Give the extent of all Plasmodium falciparum-infected red blood cells.
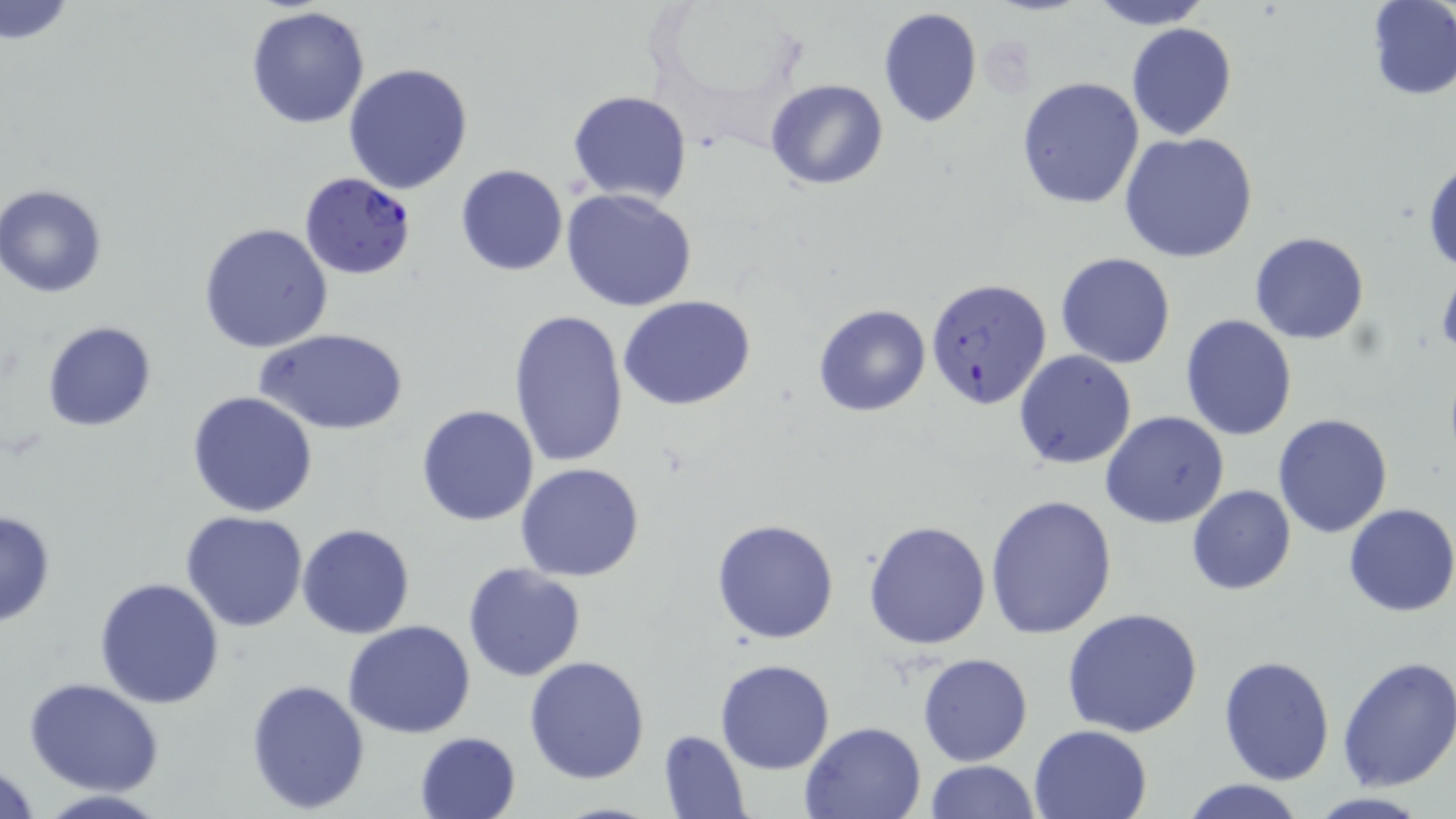
Approximate bounding boxes as [x1, y1, x2, y2] in pixels.
Plasmodium falciparum-infected red blood cells: [300, 170, 416, 278], [924, 279, 1052, 413].

Uninfected red blood cell locations: [1086, 0, 1214, 29], [1366, 0, 1455, 100], [1, 1, 75, 44], [246, 5, 372, 130], [876, 6, 983, 128], [1125, 23, 1237, 140], [343, 61, 474, 193], [1016, 77, 1146, 210], [766, 79, 889, 190], [568, 89, 692, 204], [1119, 131, 1258, 262], [1425, 161, 1456, 273], [455, 165, 569, 277], [0, 184, 109, 298], [560, 188, 699, 313], [199, 223, 334, 353], [1250, 232, 1369, 344], [1054, 252, 1177, 368], [618, 295, 757, 410], [813, 303, 931, 417], [508, 309, 629, 469], [1180, 313, 1297, 440], [43, 321, 157, 433], [258, 326, 407, 436], [1013, 349, 1137, 469], [186, 391, 319, 517], [415, 404, 539, 527], [1101, 411, 1230, 529], [1272, 413, 1395, 538], [515, 463, 646, 582], [1187, 485, 1295, 595], [983, 492, 1117, 638], [1343, 503, 1456, 616], [0, 509, 57, 628], [181, 510, 309, 631], [712, 517, 841, 643], [864, 519, 993, 650], [296, 523, 415, 639], [462, 563, 587, 682], [95, 576, 225, 707], [1061, 606, 1206, 739], [343, 620, 477, 737], [917, 653, 1033, 766], [1217, 654, 1336, 785], [524, 655, 649, 784], [715, 658, 835, 773], [1334, 658, 1456, 792], [24, 677, 165, 796], [246, 677, 372, 815], [801, 720, 927, 818], [1027, 723, 1153, 819], [658, 729, 751, 817], [414, 731, 522, 819], [0, 758, 43, 818], [922, 759, 1039, 819], [1180, 779, 1308, 819], [29, 790, 176, 819], [1300, 791, 1437, 818]. Slide-level diagnosis: Plasmodium falciparum. Image is 1456×819 pixels. May-Grünwald-Giemsa stain. Optical microscopy. Thin blood film. 1000x magnification. One field of a larger specimen.